Outline each blood parasite and name the species.
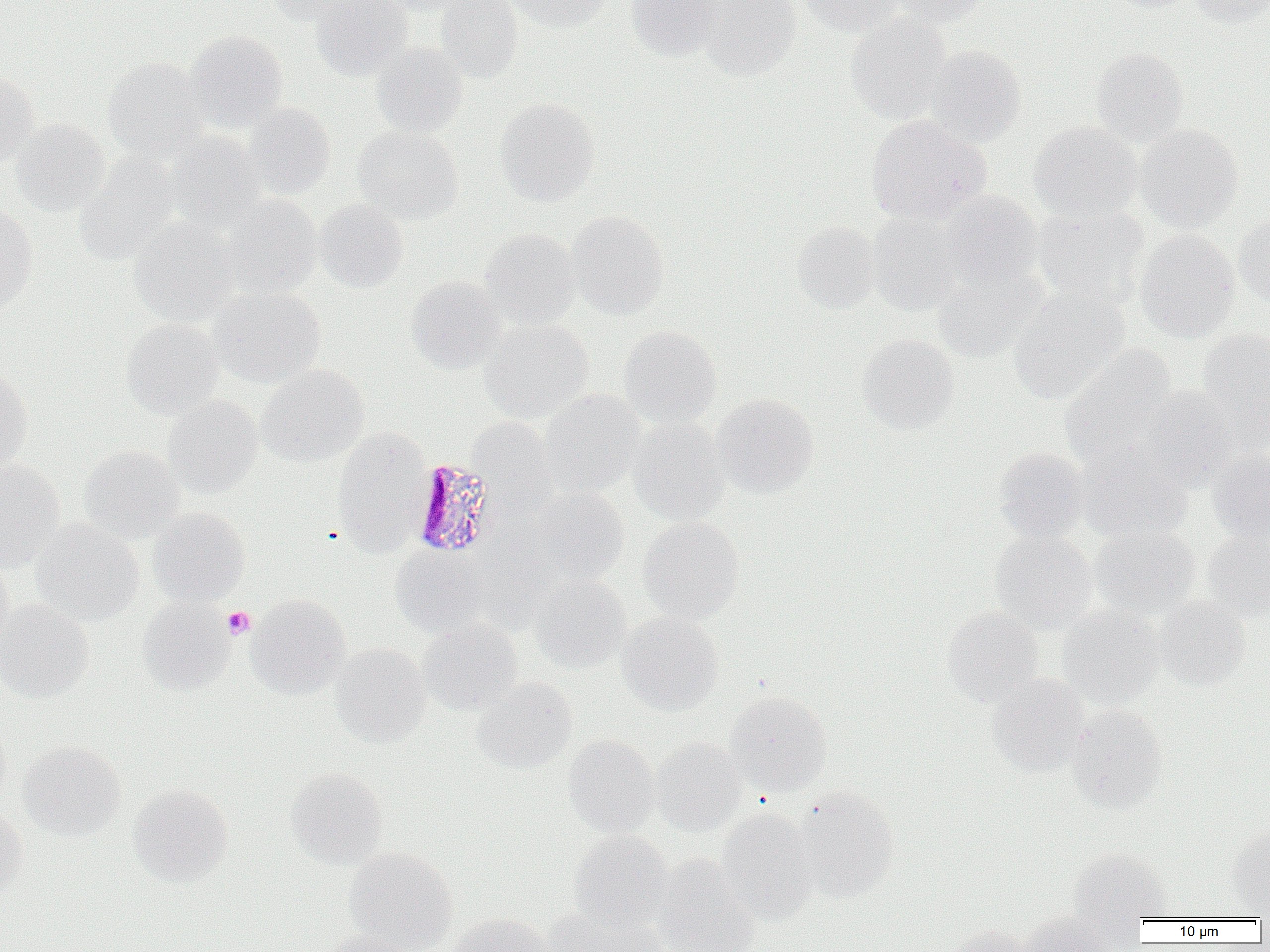
Approximate bounding boxes as (x1, y1, x2, y2) in pixels.
Plasmodium malariae-infected red blood cells: (410, 458, 501, 559).
No Plasmodium falciparum, Plasmodium ovale, Plasmodium vivax, Babesia divergens, or Trypanosoma brucei observed.

Summary:
  - Platelet locations: (222, 607, 255, 639)
  - Uninfected red blood cell locations: (263, 0, 366, 25), (312, 0, 413, 81), (375, 0, 471, 15), (435, 0, 523, 82), (507, 0, 612, 31), (626, 0, 725, 61), (693, 0, 801, 80), (798, 0, 905, 37), (889, 0, 993, 26), (1106, 0, 1198, 12), (1188, 0, 1269, 28), (846, 12, 953, 123), (184, 30, 287, 130), (370, 42, 468, 138), (925, 45, 1026, 146), (1090, 47, 1188, 147), (102, 57, 211, 161), (0, 71, 39, 168), (494, 98, 600, 206), (241, 102, 336, 199), (866, 115, 992, 224), (10, 119, 110, 217), (1028, 121, 1142, 223), (1133, 123, 1243, 232), (353, 127, 463, 224), (164, 132, 266, 231), (74, 155, 179, 264), (940, 191, 1043, 288), (222, 195, 322, 299), (315, 200, 408, 292), (0, 203, 37, 312), (1031, 204, 1149, 307), (567, 210, 669, 319), (865, 211, 968, 316), (1234, 213, 1270, 308), (130, 217, 239, 325), (791, 221, 881, 313), (479, 228, 581, 328), (1135, 229, 1240, 342), (930, 262, 1049, 361), (405, 276, 506, 374), (1008, 286, 1129, 404), (209, 287, 325, 387), (121, 319, 223, 419), (479, 319, 593, 422), (619, 326, 722, 429), (1195, 327, 1270, 442), (856, 334, 960, 435), (1059, 345, 1177, 468), (257, 365, 368, 467), (0, 369, 33, 472), (1137, 385, 1240, 487), (538, 389, 646, 498), (711, 393, 818, 497), (162, 395, 263, 497), (468, 417, 556, 508), (627, 418, 731, 524), (332, 429, 432, 555), (79, 445, 185, 542), (994, 447, 1090, 543), (1207, 448, 1270, 545), (1077, 450, 1192, 543), (0, 460, 65, 571), (527, 487, 629, 587), (148, 507, 250, 606), (638, 516, 744, 623), (30, 519, 144, 625), (1090, 525, 1200, 620), (1203, 530, 1270, 620), (990, 532, 1098, 633), (390, 546, 489, 637), (0, 559, 14, 655), (529, 575, 629, 673), (246, 594, 350, 698), (1153, 597, 1250, 690), (138, 598, 235, 695), (0, 599, 95, 702), (1057, 606, 1164, 708), (941, 607, 1044, 707), (617, 612, 723, 715), (418, 620, 523, 714), (331, 643, 430, 747), (987, 674, 1091, 776), (472, 677, 577, 773), (725, 690, 832, 796), (1066, 704, 1167, 811), (0, 720, 11, 809), (563, 735, 659, 836), (650, 737, 746, 836), (18, 741, 125, 840), (285, 768, 387, 867), (128, 784, 233, 887), (790, 788, 899, 902), (0, 808, 28, 900), (716, 808, 820, 923), (1227, 828, 1270, 918), (569, 831, 673, 929), (1068, 847, 1171, 928), (344, 848, 458, 952), (651, 856, 761, 952), (547, 905, 668, 952), (1017, 912, 1117, 952), (445, 913, 553, 952), (942, 925, 1031, 952), (321, 930, 422, 952)
  - Slide-level diagnosis: Plasmodium malariae
  - Modality: optical microscopy
  - Preparation: thin blood smear
  - Magnification: 1000x
  - Field of view: one of a larger specimen
  - Image size: 1270×952 pixels